State which parasite is depicted.
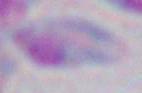

This is Toxoplasma gondii.

magnification = 1000x
modality = micrograph